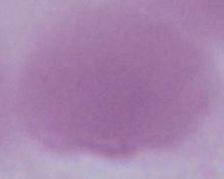

modality: micrograph
magnification: 1000x
identification: erythrocyte